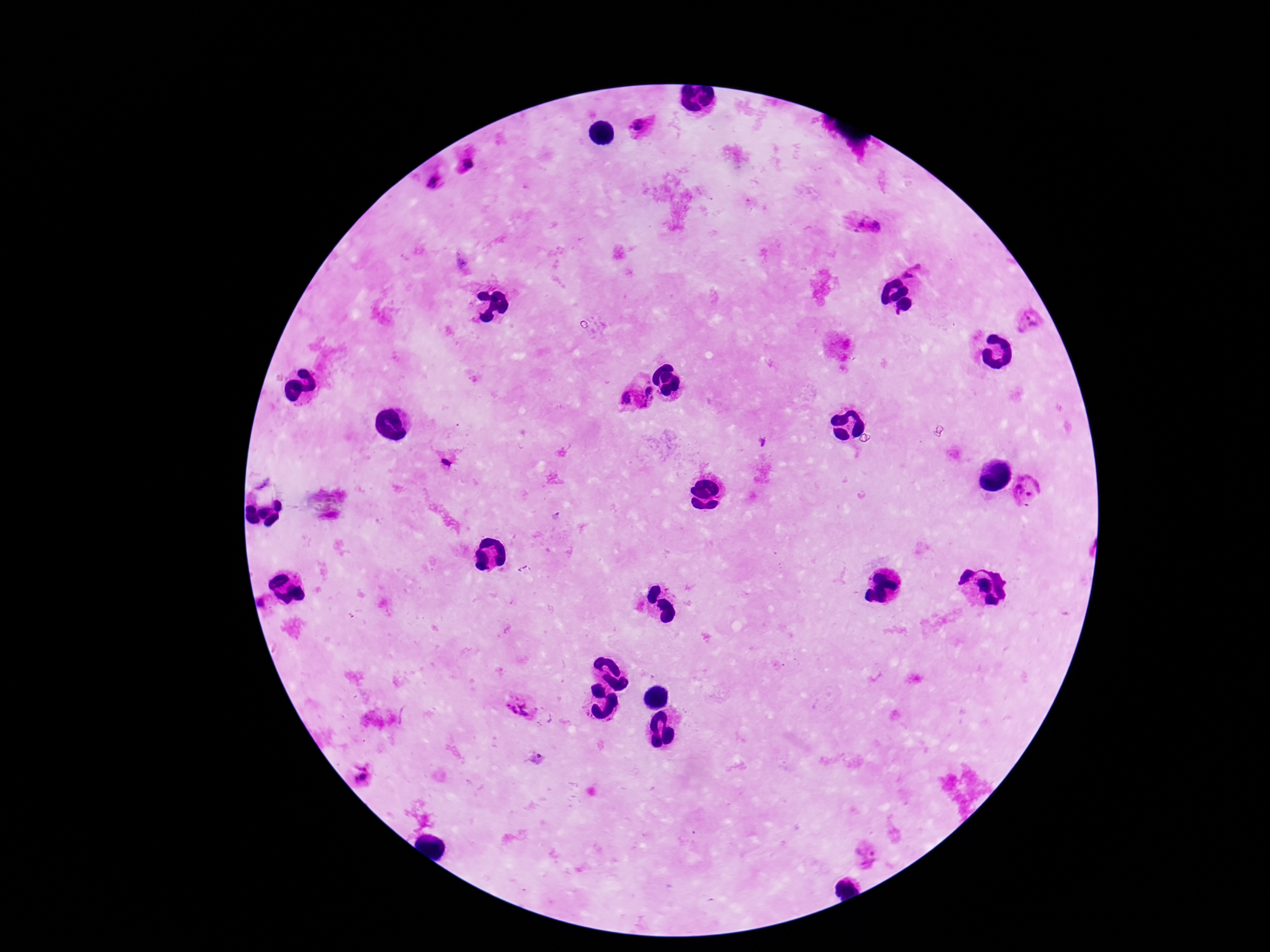
Approximate centers as (x, y) in pixels.
Summary:
  - Plasmodium parasite locations: (638, 126), (472, 163), (431, 178), (856, 221), (877, 225), (912, 271), (1029, 321), (647, 393), (626, 398), (1029, 491), (520, 705), (365, 773), (864, 855)
  - Field of view: one from this slide
  - Magnification: 100x
  - Image size: 1270×952 pixels
  - Capture: smartphone camera through the microscope eyepiece
  - Preparation: thick blood smear
  - Patient malaria status: infected
  - Stain: Giemsa